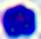
magnification = 400x
modality = micrograph
identification = leukocyte